Locate and identify every blood parasite.
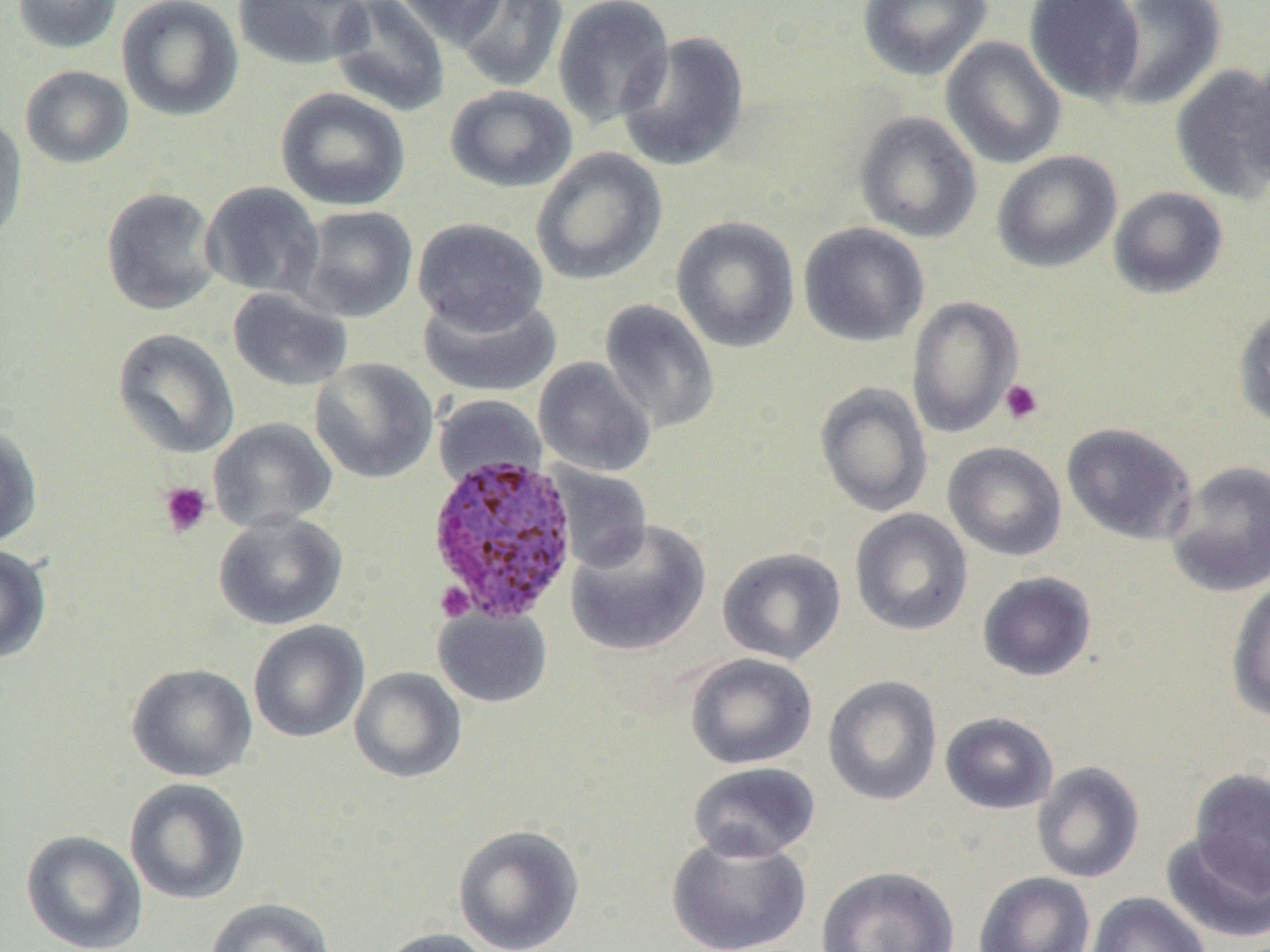
Approximate bounding boxes as [x1, y1, x2, y2] in pixels.
Plasmodium ovale-infected red blood cells: [425, 453, 580, 622].
No Plasmodium falciparum, Plasmodium malariae, Plasmodium vivax, Babesia divergens, or Trypanosoma brucei observed.

Summary:
  - Uninfected red blood cell locations: [11, 0, 123, 53], [117, 0, 244, 121], [233, 0, 371, 70], [328, 0, 450, 117], [393, 0, 508, 49], [454, 0, 568, 92], [552, 0, 675, 130], [857, 0, 992, 81], [1024, 0, 1145, 105], [1105, 0, 1227, 111], [615, 30, 750, 172], [940, 36, 1066, 170], [1248, 54, 1270, 191], [1169, 64, 1270, 204], [19, 65, 134, 169], [444, 84, 578, 193], [275, 87, 411, 211], [854, 111, 982, 243], [0, 113, 28, 247], [530, 147, 667, 286], [992, 150, 1122, 273], [200, 181, 324, 300], [100, 186, 222, 316], [1108, 186, 1229, 299], [295, 205, 418, 323], [671, 216, 801, 353], [412, 217, 549, 333], [798, 222, 930, 347], [227, 287, 353, 392], [417, 289, 563, 398], [906, 295, 1024, 438], [599, 299, 720, 434], [1232, 300, 1270, 432], [111, 327, 240, 459], [534, 357, 656, 477], [310, 358, 439, 484], [815, 382, 933, 517], [432, 394, 546, 490], [208, 417, 338, 533], [1061, 422, 1197, 545], [0, 423, 43, 549], [943, 442, 1067, 561], [1165, 460, 1270, 598], [547, 463, 653, 572], [850, 509, 973, 636], [212, 512, 349, 630], [566, 519, 712, 657], [0, 544, 52, 663], [717, 547, 847, 665], [977, 571, 1097, 682], [1226, 578, 1270, 723], [433, 606, 552, 708], [248, 621, 370, 744], [684, 653, 818, 770], [126, 663, 257, 782], [349, 667, 467, 784], [823, 675, 943, 806], [940, 712, 1059, 814], [1033, 761, 1145, 884], [688, 762, 821, 863], [1189, 768, 1270, 894], [123, 778, 251, 906], [453, 824, 585, 952], [20, 829, 148, 952], [1161, 829, 1270, 943], [666, 833, 812, 952], [816, 865, 960, 952], [974, 871, 1096, 952], [1085, 892, 1211, 952], [205, 898, 338, 952], [373, 927, 498, 952]
  - Platelet locations: [999, 379, 1043, 425], [157, 480, 213, 538], [435, 582, 474, 623]
  - Slide-level diagnosis: Plasmodium ovale
  - Magnification: 1000x
  - Image size: 1270×952 pixels
  - Field of view: one of a larger specimen
  - Modality: optical microscopy
  - Preparation: thin blood smear